Give the preparation type.
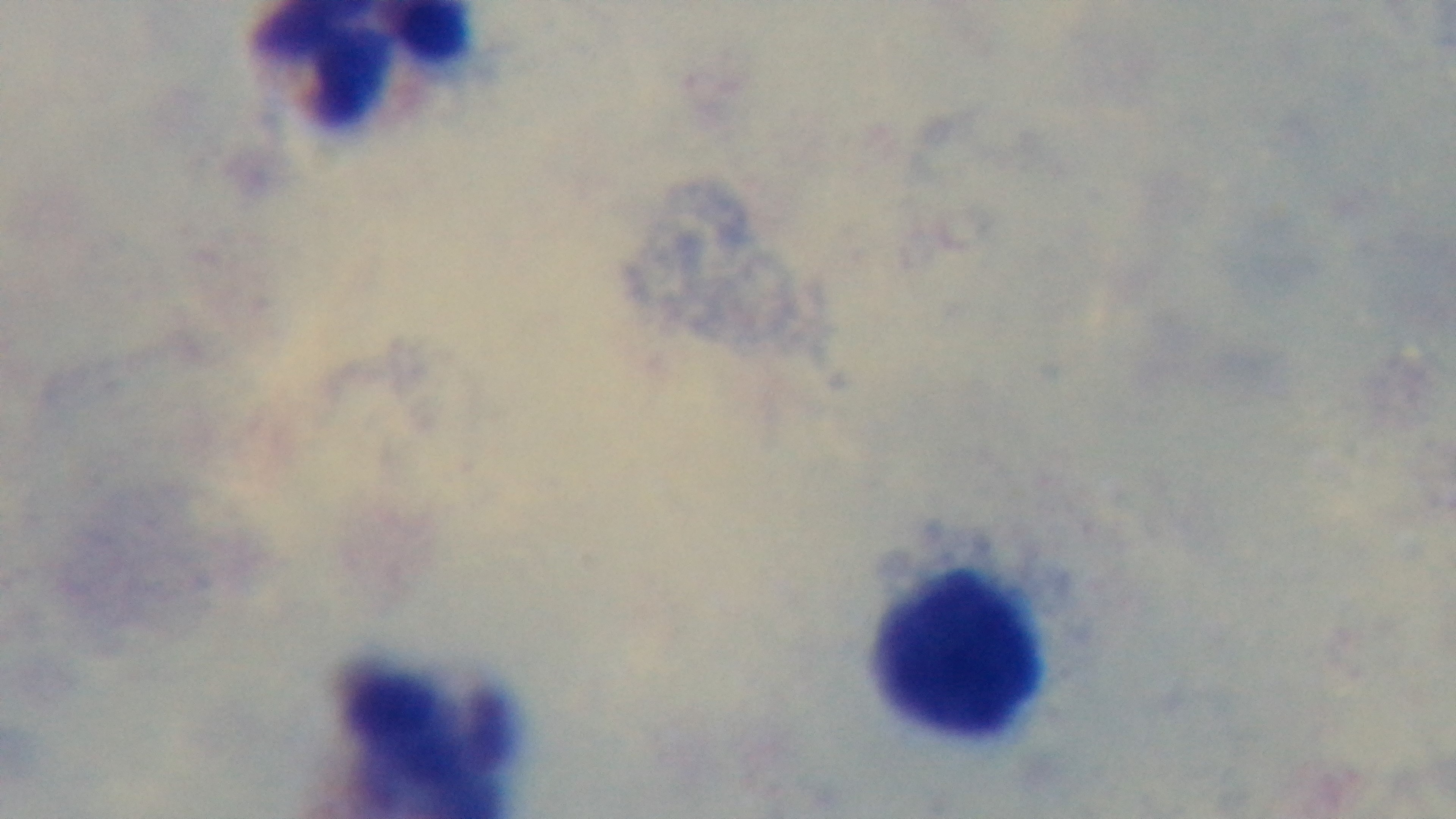

Thick.

Mounted 4K digital camera. Giemsa stain. Malaria status: uninfected. Oil-immersion objective, 100x. Light microscopy. One field from the slide.